Name the parasite shown.
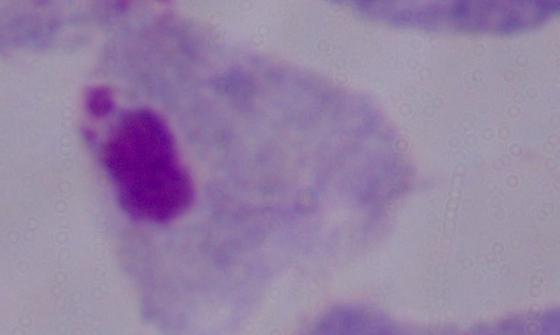

A trichomonad.

Micrograph. Captured at 1000x magnification.